Locate and identify every blood parasite.
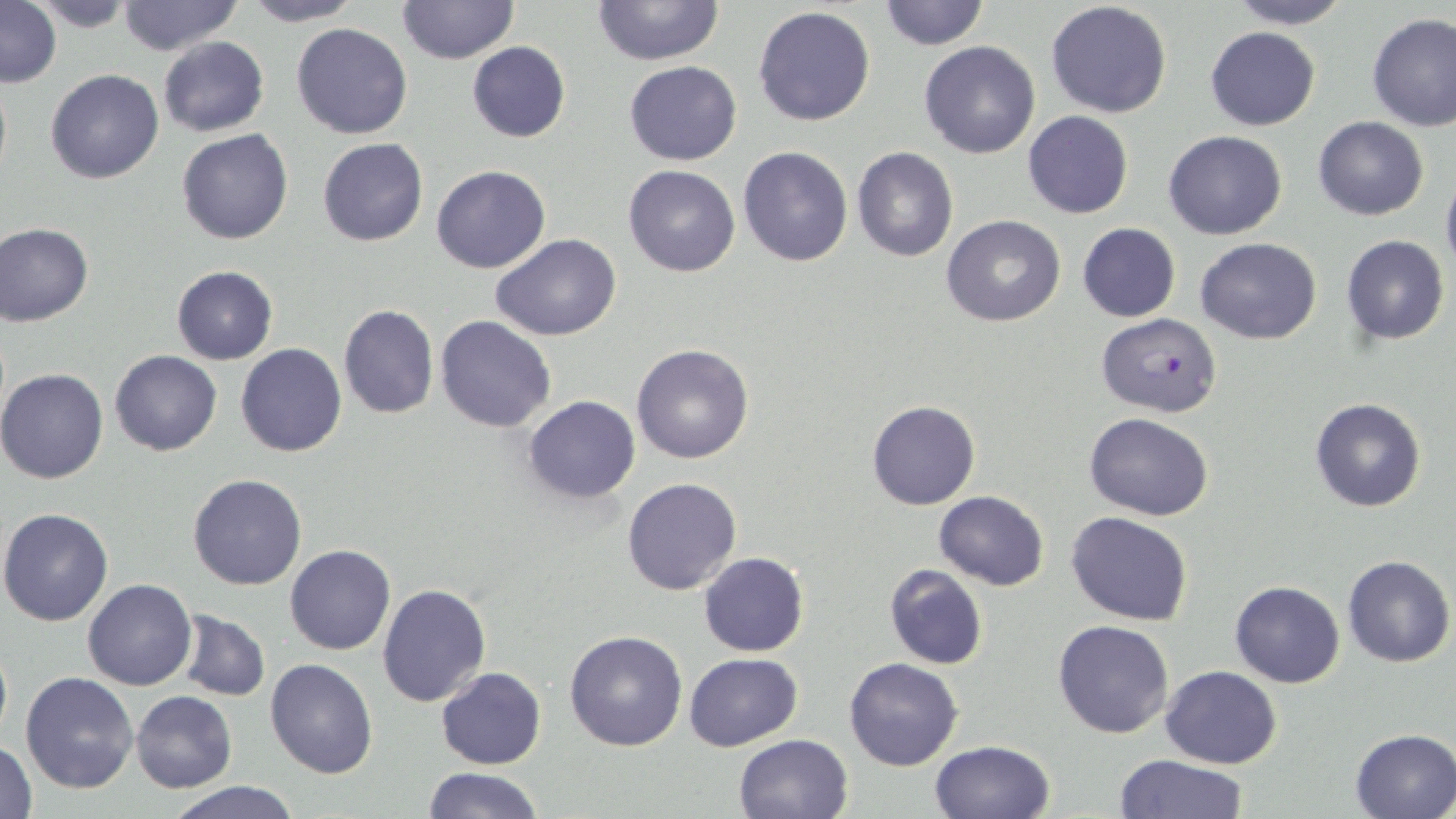
Approximate bounding boxes as (x1, y1, x2, y2) in pixels.
Plasmodium falciparum-infected red blood cells: (1096, 313, 1221, 417).
No Plasmodium ovale, Plasmodium malariae, Plasmodium vivax, Babesia divergens, or Trypanosoma brucei observed.

{
  "slide_level_diagnosis": "Plasmodium falciparum",
  "image_size": "1456×819 pixels",
  "uninfected_red_blood_cell_locations": "approximate bounding boxes as (x1, y1, x2, y2) in pixels: (29, 0, 138, 30), (240, 0, 364, 26), (398, 0, 517, 64), (593, 0, 724, 66), (876, 0, 989, 51), (1222, 0, 1354, 29), (116, 1, 241, 55), (1045, 1, 1173, 119), (1, 2, 60, 86), (752, 6, 877, 127), (1366, 12, 1456, 131), (292, 23, 412, 140), (1204, 27, 1320, 130), (158, 36, 270, 137), (918, 40, 1041, 159), (466, 41, 571, 143), (624, 61, 742, 165), (46, 69, 163, 183), (1022, 111, 1133, 219), (1312, 117, 1430, 220), (176, 129, 293, 245), (1163, 131, 1287, 240), (318, 138, 428, 247), (738, 146, 853, 266), (853, 148, 958, 262), (622, 164, 740, 277), (431, 166, 551, 274), (1441, 170, 1456, 282), (942, 215, 1067, 328), (0, 221, 95, 326), (1076, 222, 1181, 322), (491, 234, 622, 342), (1341, 234, 1450, 345), (1196, 238, 1323, 344), (171, 265, 277, 364), (338, 303, 439, 419), (435, 314, 557, 432), (237, 344, 348, 457), (631, 344, 755, 464), (109, 350, 223, 456), (0, 367, 109, 485), (522, 396, 641, 504), (1309, 397, 1428, 513), (867, 400, 980, 510), (1084, 412, 1213, 522), (188, 473, 308, 591), (622, 477, 742, 595), (935, 491, 1049, 590), (0, 507, 115, 626), (1066, 512, 1194, 626), (286, 543, 396, 655), (698, 553, 809, 657), (1342, 555, 1455, 667), (883, 563, 988, 671), (83, 578, 196, 690), (1230, 579, 1345, 688), (376, 583, 489, 706), (178, 612, 269, 700), (1053, 619, 1175, 739), (565, 630, 687, 750), (0, 634, 12, 749), (685, 653, 802, 749), (844, 656, 963, 771), (265, 659, 378, 779), (1160, 665, 1282, 769), (436, 667, 546, 769), (20, 671, 140, 794), (132, 690, 237, 793), (1350, 728, 1456, 817), (733, 733, 854, 819), (929, 740, 1056, 819), (1, 741, 38, 819), (1115, 753, 1246, 819), (421, 766, 544, 819), (167, 780, 301, 819)",
  "magnification": "1000x",
  "modality": "light microscopy",
  "field_of_view": "single",
  "stain": "May-Grünwald-Giemsa",
  "preparation": "thin blood smear"
}